Identify the blood parasite species.
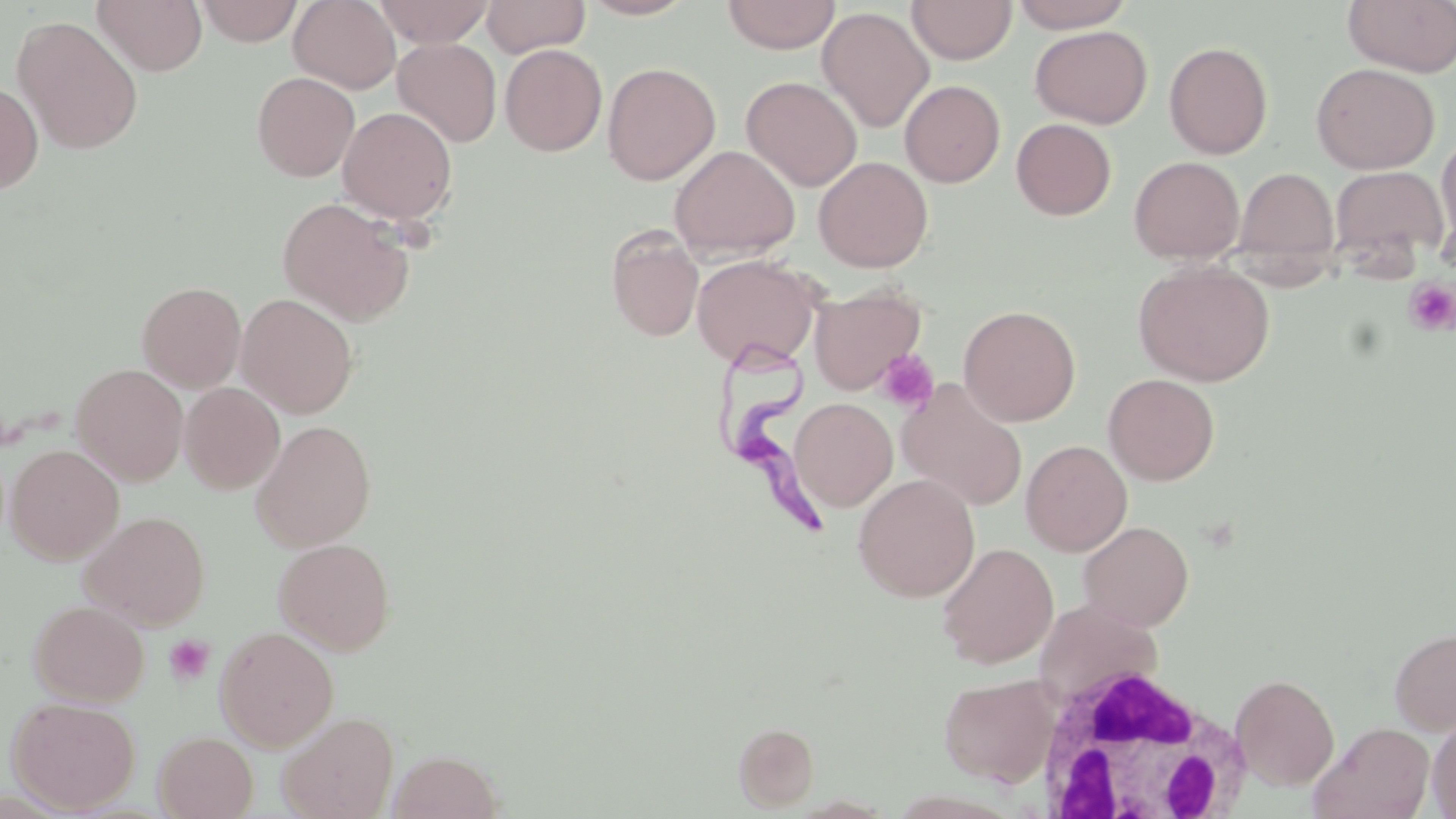
Trypanosoma brucei.

Summary:
  - Coordinate format: approximate bounding boxes as [x1, y1, x2, y2] in pixels
  - White blood cell locations: [1031, 662, 1251, 817]
  - Trypanosoma brucei locations: [717, 338, 826, 537]
  - Uninfected red blood cell locations: [92, 0, 207, 76], [288, 0, 401, 94], [374, 0, 494, 47], [481, 0, 590, 58], [578, 0, 698, 20], [722, 0, 841, 54], [907, 0, 1016, 64], [1008, 0, 1136, 32], [1342, 0, 1456, 76], [195, 1, 303, 46], [816, 7, 934, 133], [12, 16, 144, 155], [1030, 25, 1152, 128], [393, 38, 502, 147], [1163, 41, 1273, 159], [500, 44, 607, 156], [602, 62, 721, 185], [1311, 62, 1440, 174], [252, 72, 360, 182], [741, 75, 863, 192], [900, 80, 1005, 187], [0, 82, 44, 196], [338, 106, 458, 225], [1012, 118, 1116, 220], [1435, 133, 1456, 252], [669, 144, 800, 262], [1129, 155, 1244, 263], [813, 156, 933, 272], [1330, 164, 1448, 268], [1233, 167, 1339, 272], [277, 197, 416, 326], [607, 228, 704, 342], [692, 253, 822, 368], [1133, 261, 1274, 386], [136, 281, 246, 393], [809, 284, 926, 395], [236, 293, 358, 418], [958, 304, 1081, 427], [70, 363, 189, 486], [1103, 373, 1220, 485], [896, 379, 1028, 512], [180, 382, 285, 495], [790, 398, 897, 512], [251, 420, 376, 552], [1020, 440, 1132, 556], [6, 444, 125, 564], [853, 473, 980, 602], [80, 510, 210, 630], [1078, 520, 1194, 630], [273, 537, 396, 655], [936, 542, 1058, 669], [1034, 597, 1162, 706], [28, 600, 149, 707], [214, 626, 338, 751], [1389, 627, 1456, 735], [938, 673, 1059, 786], [1230, 674, 1340, 790], [7, 696, 140, 813], [277, 710, 400, 819], [1427, 716, 1456, 817], [734, 721, 819, 811], [1309, 722, 1435, 819], [153, 731, 257, 818], [388, 750, 503, 819]
  - Platelet locations: [1404, 278, 1456, 336], [875, 349, 940, 413], [164, 634, 215, 687]
  - Modality: optical microscopy
  - Image size: 1456×819 pixels
  - Preparation: thin blood film
  - Stain: May-Grünwald-Giemsa
  - Field of view: one of a larger specimen
  - Magnification: 1000x